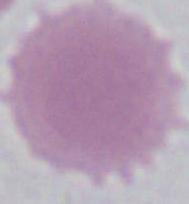

Micrograph. A red blood cell is seen. Captured at 1000x magnification.